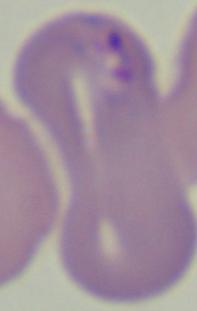
modality = micrograph
magnification = 1000x
identification = Babesia